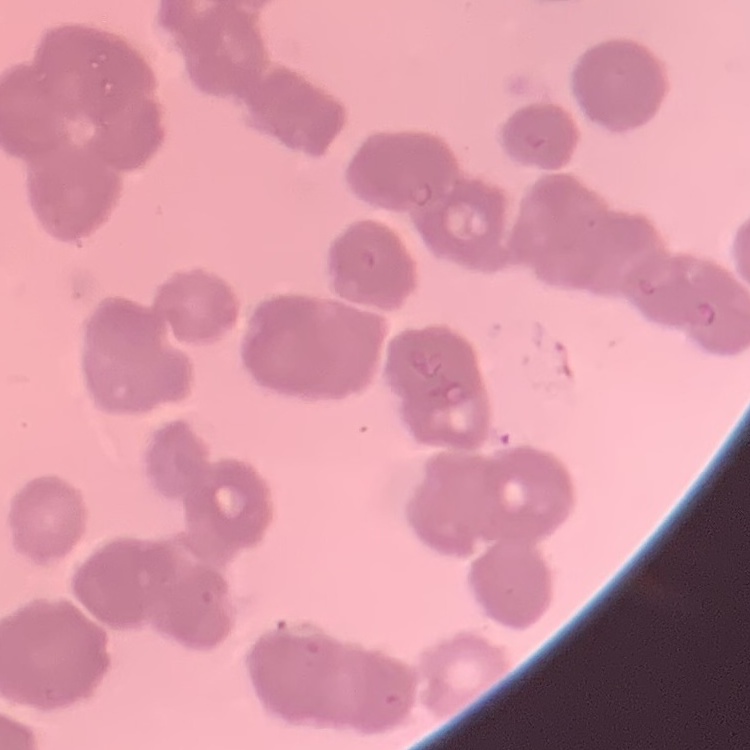
red blood cell morphology = rouleaux formation
image type = square crop of a larger photomicrograph
preparation = thin peripheral smear
stain = Field's or Giemsa